Give the extent of all Plasmodium ovale-infected red blood cells.
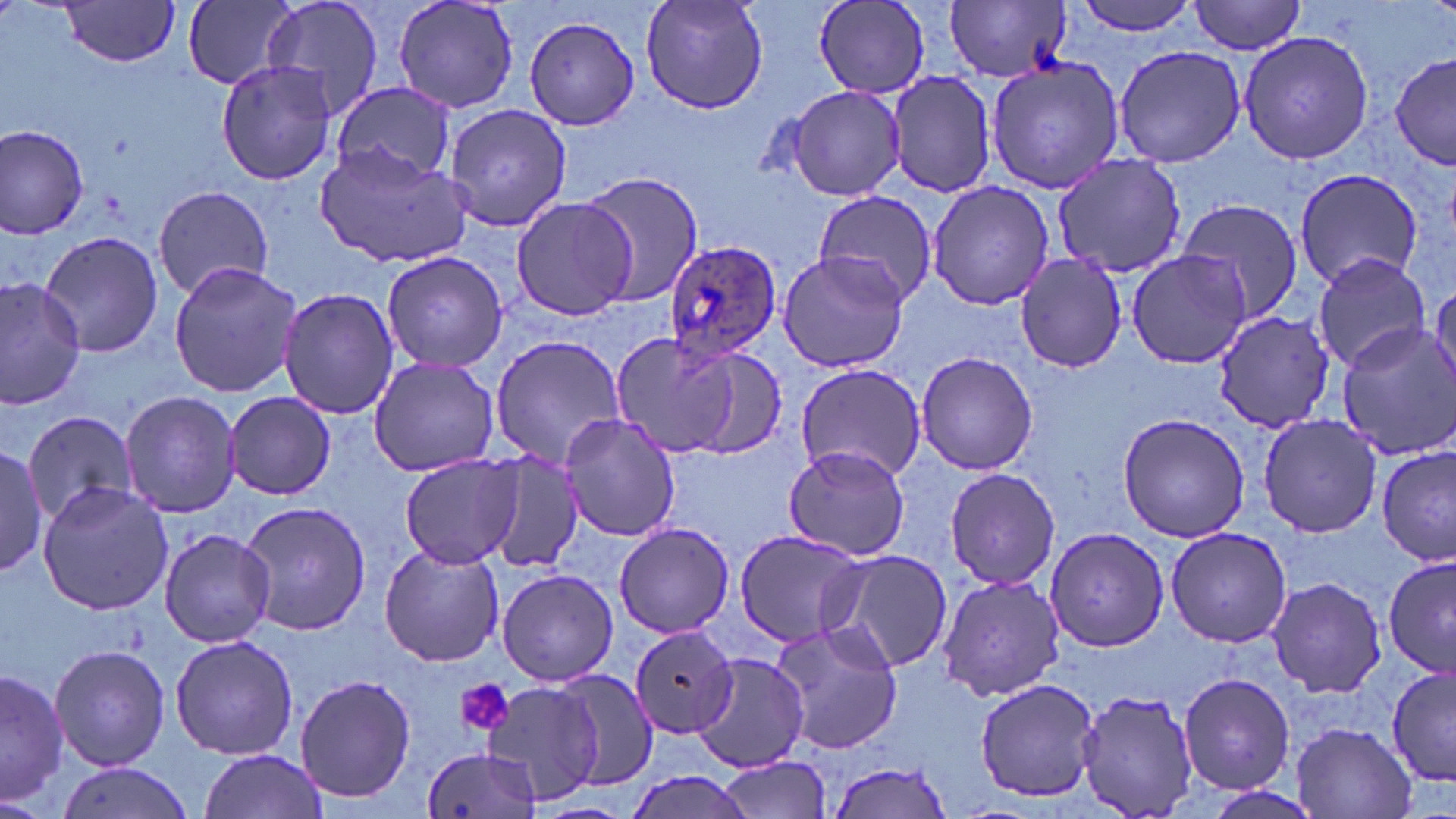
Approximate bounding boxes as (x1, y1, x2, y2) in pixels.
Plasmodium ovale-infected red blood cells: (660, 240, 784, 360).

Platelet locations: (457, 680, 514, 737). Uninfected red blood cell locations: (260, 0, 387, 123), (391, 0, 520, 113), (639, 0, 768, 114), (1070, 0, 1206, 36), (56, 1, 183, 65), (183, 1, 300, 90), (812, 1, 930, 100), (946, 1, 1071, 84), (1190, 1, 1307, 55), (523, 15, 641, 130), (1237, 29, 1374, 167), (1113, 45, 1245, 169), (1393, 52, 1456, 167), (985, 56, 1128, 194), (216, 61, 336, 183), (886, 69, 996, 198), (331, 82, 455, 183), (781, 86, 908, 202), (443, 102, 572, 232), (0, 121, 91, 239), (314, 143, 475, 269), (1051, 153, 1184, 281), (1292, 167, 1425, 290), (577, 171, 702, 307), (927, 180, 1056, 311), (152, 185, 275, 299), (811, 190, 939, 309), (509, 195, 635, 320), (1176, 196, 1307, 328), (39, 232, 163, 358), (380, 250, 510, 374), (777, 250, 911, 374), (1014, 250, 1129, 372), (1126, 250, 1250, 370), (1311, 250, 1431, 375), (167, 261, 302, 397), (0, 276, 87, 409), (1429, 286, 1456, 391), (277, 287, 401, 421), (1211, 312, 1333, 434), (1336, 324, 1456, 461), (604, 334, 777, 463), (489, 335, 628, 465), (915, 349, 1039, 477), (367, 355, 500, 478), (795, 362, 925, 483), (119, 388, 241, 518), (223, 392, 335, 499), (22, 409, 138, 527), (1115, 411, 1253, 543), (1257, 411, 1384, 538), (558, 413, 681, 540), (0, 443, 50, 574), (783, 446, 911, 562), (1375, 446, 1455, 564), (481, 451, 586, 572), (399, 452, 522, 569), (942, 466, 1063, 592), (35, 482, 173, 615), (238, 500, 373, 636), (614, 523, 737, 638), (1163, 525, 1292, 647), (1043, 528, 1169, 652), (158, 529, 276, 647), (735, 530, 866, 645), (377, 543, 505, 667), (816, 548, 953, 676), (1381, 555, 1456, 675), (496, 569, 619, 685), (936, 572, 1066, 702), (1266, 576, 1388, 698), (768, 620, 906, 754), (623, 626, 750, 755), (169, 634, 299, 760), (49, 643, 170, 771), (687, 650, 813, 770), (1387, 664, 1455, 788), (1, 668, 69, 806), (546, 668, 659, 789), (295, 672, 416, 805), (1176, 672, 1295, 794), (972, 678, 1104, 802), (482, 679, 603, 805), (1074, 689, 1203, 819), (1289, 721, 1420, 819), (422, 743, 542, 819), (196, 748, 330, 818), (715, 756, 831, 819), (54, 758, 189, 819), (827, 760, 956, 818), (624, 771, 757, 819). Slide-level diagnosis: Plasmodium ovale. Thin blood film. May-Grünwald-Giemsa stain. 1000x magnification. Image is 1456×819 pixels. One field of a larger specimen. Light microscopy.